Classify this cell by malaria status.
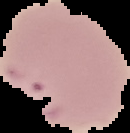
Parasitized.

From a thin blood smear. Cell region segmented out of the field of view; the surrounding area is masked to black. Image is 130×133 pixels.